Outline each Plasmodium falciparum-infected red blood cell.
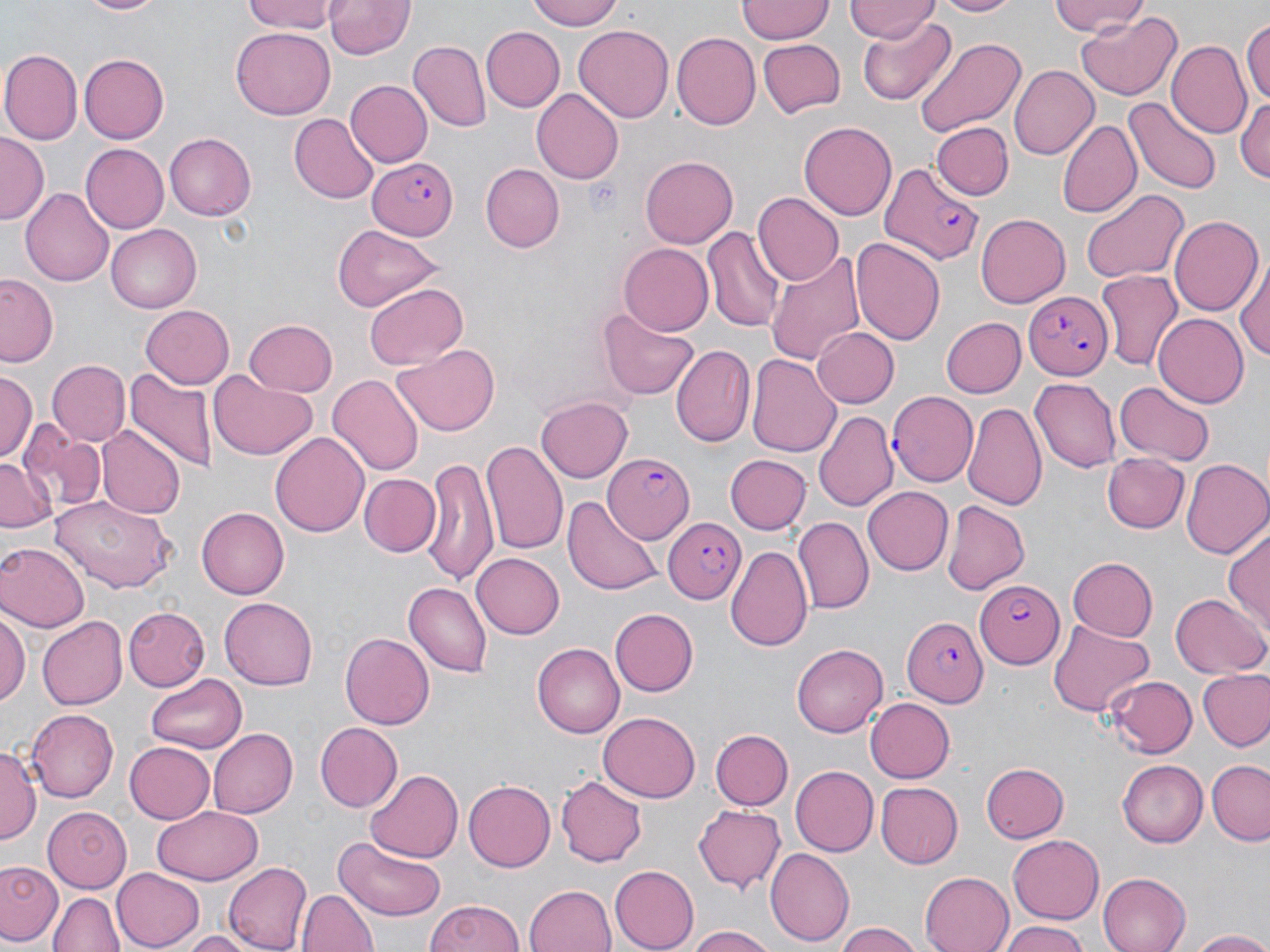

Approximate bounding boxes as named x1/y1/x2/y2 corners in pixels.
Plasmodium falciparum-infected red blood cells: (x1=369, y1=158, x2=459, y2=238), (x1=879, y1=163, x2=986, y2=264), (x1=1024, y1=293, x2=1114, y2=377), (x1=887, y1=391, x2=976, y2=488), (x1=604, y1=453, x2=694, y2=544), (x1=664, y1=516, x2=749, y2=600), (x1=975, y1=580, x2=1064, y2=669), (x1=901, y1=616, x2=988, y2=707).

slide-level diagnosis = Plasmodium falciparum
stain = May-Grünwald-Giemsa
preparation = thin blood film
image size = 1270×952 pixels
modality = optical microscopy
magnification = 1000x
uninfected red blood cell locations = approximate bounding boxes as named x1/y1/x2/y2 corners in pixels: (x1=74, y1=0, x2=167, y2=17), (x1=238, y1=0, x2=340, y2=35), (x1=527, y1=0, x2=626, y2=30), (x1=738, y1=0, x2=834, y2=42), (x1=927, y1=0, x2=1025, y2=18), (x1=1049, y1=0, x2=1151, y2=37), (x1=325, y1=1, x2=414, y2=61), (x1=848, y1=1, x2=938, y2=43), (x1=1076, y1=12, x2=1182, y2=101), (x1=1242, y1=13, x2=1270, y2=112), (x1=858, y1=16, x2=958, y2=107), (x1=575, y1=25, x2=674, y2=122), (x1=479, y1=26, x2=563, y2=111), (x1=230, y1=28, x2=334, y2=118), (x1=672, y1=33, x2=761, y2=128), (x1=757, y1=37, x2=845, y2=117), (x1=914, y1=37, x2=1028, y2=142), (x1=410, y1=42, x2=492, y2=131), (x1=1168, y1=42, x2=1251, y2=141), (x1=3, y1=50, x2=82, y2=143), (x1=80, y1=53, x2=169, y2=142), (x1=1009, y1=62, x2=1099, y2=158), (x1=344, y1=80, x2=432, y2=168), (x1=531, y1=88, x2=625, y2=185), (x1=1236, y1=93, x2=1270, y2=185), (x1=1124, y1=96, x2=1221, y2=194), (x1=288, y1=115, x2=378, y2=203), (x1=1059, y1=119, x2=1141, y2=218), (x1=799, y1=120, x2=897, y2=222), (x1=932, y1=122, x2=1013, y2=201), (x1=165, y1=132, x2=257, y2=220), (x1=0, y1=134, x2=48, y2=221), (x1=80, y1=142, x2=169, y2=234), (x1=641, y1=155, x2=738, y2=249), (x1=480, y1=163, x2=563, y2=251), (x1=21, y1=187, x2=114, y2=286), (x1=1082, y1=190, x2=1190, y2=283), (x1=754, y1=192, x2=843, y2=284), (x1=976, y1=213, x2=1071, y2=307), (x1=1169, y1=215, x2=1262, y2=317), (x1=104, y1=224, x2=200, y2=312), (x1=329, y1=225, x2=447, y2=310), (x1=703, y1=228, x2=787, y2=333), (x1=852, y1=236, x2=946, y2=347), (x1=619, y1=241, x2=715, y2=334), (x1=765, y1=249, x2=867, y2=365), (x1=1234, y1=254, x2=1270, y2=368), (x1=1097, y1=271, x2=1181, y2=370), (x1=1, y1=275, x2=61, y2=365), (x1=364, y1=284, x2=467, y2=370), (x1=139, y1=305, x2=234, y2=388), (x1=599, y1=309, x2=700, y2=400), (x1=1152, y1=314, x2=1248, y2=407), (x1=938, y1=316, x2=1025, y2=398), (x1=243, y1=319, x2=338, y2=396), (x1=813, y1=328, x2=899, y2=406), (x1=671, y1=344, x2=753, y2=447), (x1=393, y1=346, x2=500, y2=437), (x1=748, y1=353, x2=841, y2=458), (x1=45, y1=359, x2=131, y2=448), (x1=125, y1=370, x2=216, y2=476), (x1=0, y1=372, x2=37, y2=465), (x1=208, y1=372, x2=318, y2=461), (x1=329, y1=374, x2=422, y2=478), (x1=1030, y1=378, x2=1119, y2=473), (x1=1116, y1=382, x2=1214, y2=463), (x1=536, y1=397, x2=633, y2=483), (x1=965, y1=400, x2=1047, y2=512), (x1=814, y1=410, x2=897, y2=510), (x1=17, y1=418, x2=105, y2=514), (x1=96, y1=426, x2=185, y2=519), (x1=271, y1=431, x2=369, y2=538), (x1=482, y1=439, x2=567, y2=555), (x1=1104, y1=452, x2=1188, y2=534), (x1=0, y1=453, x2=54, y2=532), (x1=725, y1=454, x2=810, y2=535), (x1=422, y1=458, x2=498, y2=584), (x1=1181, y1=459, x2=1270, y2=557), (x1=362, y1=473, x2=439, y2=554), (x1=864, y1=487, x2=953, y2=576), (x1=566, y1=492, x2=661, y2=596), (x1=51, y1=496, x2=176, y2=593), (x1=941, y1=500, x2=1030, y2=594), (x1=197, y1=507, x2=288, y2=600), (x1=792, y1=518, x2=873, y2=615), (x1=1224, y1=524, x2=1269, y2=633), (x1=0, y1=542, x2=86, y2=632), (x1=726, y1=544, x2=813, y2=655), (x1=471, y1=553, x2=563, y2=639), (x1=1068, y1=557, x2=1159, y2=639), (x1=404, y1=582, x2=492, y2=677), (x1=1172, y1=593, x2=1267, y2=680), (x1=220, y1=596, x2=319, y2=689), (x1=122, y1=605, x2=208, y2=690), (x1=0, y1=607, x2=28, y2=715), (x1=613, y1=608, x2=700, y2=696), (x1=38, y1=615, x2=127, y2=709), (x1=1049, y1=619, x2=1154, y2=716), (x1=340, y1=631, x2=434, y2=730), (x1=793, y1=642, x2=889, y2=738), (x1=532, y1=644, x2=624, y2=738), (x1=1199, y1=669, x2=1270, y2=748), (x1=147, y1=675, x2=247, y2=755), (x1=1107, y1=675, x2=1195, y2=756), (x1=865, y1=697, x2=955, y2=783), (x1=26, y1=708, x2=117, y2=803), (x1=598, y1=712, x2=701, y2=802), (x1=314, y1=722, x2=403, y2=811), (x1=207, y1=726, x2=297, y2=818), (x1=710, y1=729, x2=793, y2=809), (x1=124, y1=740, x2=215, y2=823), (x1=0, y1=747, x2=41, y2=845), (x1=1118, y1=760, x2=1208, y2=848), (x1=1209, y1=760, x2=1270, y2=845), (x1=979, y1=762, x2=1068, y2=842), (x1=789, y1=764, x2=877, y2=854), (x1=364, y1=766, x2=467, y2=862), (x1=555, y1=773, x2=647, y2=867), (x1=463, y1=779, x2=555, y2=871), (x1=876, y1=781, x2=961, y2=869), (x1=694, y1=805, x2=787, y2=895), (x1=42, y1=807, x2=131, y2=894), (x1=153, y1=807, x2=264, y2=885), (x1=334, y1=835, x2=447, y2=920), (x1=1007, y1=835, x2=1103, y2=924), (x1=767, y1=847, x2=855, y2=944), (x1=1, y1=859, x2=63, y2=947), (x1=223, y1=861, x2=312, y2=951), (x1=609, y1=865, x2=699, y2=950), (x1=110, y1=867, x2=204, y2=950), (x1=920, y1=871, x2=1013, y2=952), (x1=1095, y1=871, x2=1190, y2=952), (x1=524, y1=883, x2=618, y2=952), (x1=299, y1=888, x2=377, y2=952), (x1=49, y1=891, x2=124, y2=952), (x1=423, y1=898, x2=527, y2=952), (x1=995, y1=921, x2=1090, y2=952), (x1=688, y1=925, x2=780, y2=952), (x1=836, y1=925, x2=925, y2=952), (x1=1185, y1=929, x2=1270, y2=951), (x1=179, y1=931, x2=257, y2=951)
field of view = one of a larger specimen